Identify the parasite.
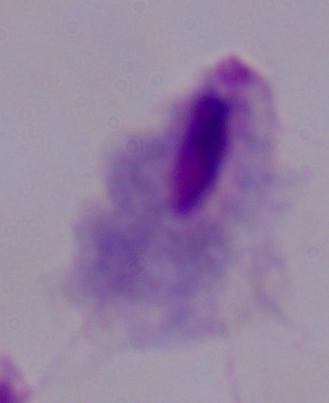
This is a trichomonad.

magnification = 1000x
modality = photomicrograph